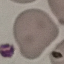
Summary:
  - Result: negative for malaria parasites
  - Preparation: thin blood film
  - Image type: automatically extracted cell patch, resized to 64 × 64 pixels
  - Capture: smartphone through the microscope eyepiece
  - Stain: Giemsa